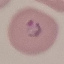

Malaria status: parasitized. Thin blood film. Giemsa-stained preparation. Acquired by smartphone through the microscope eyepiece. Automatically extracted cell patch, resized to 64 × 64 pixels.